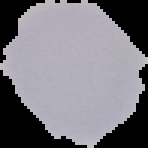
{
  "malaria_status": "uninfected",
  "image_size": "148×148 pixels",
  "image_type": "segmented cell region on a black background",
  "preparation": "thin blood smear"
}